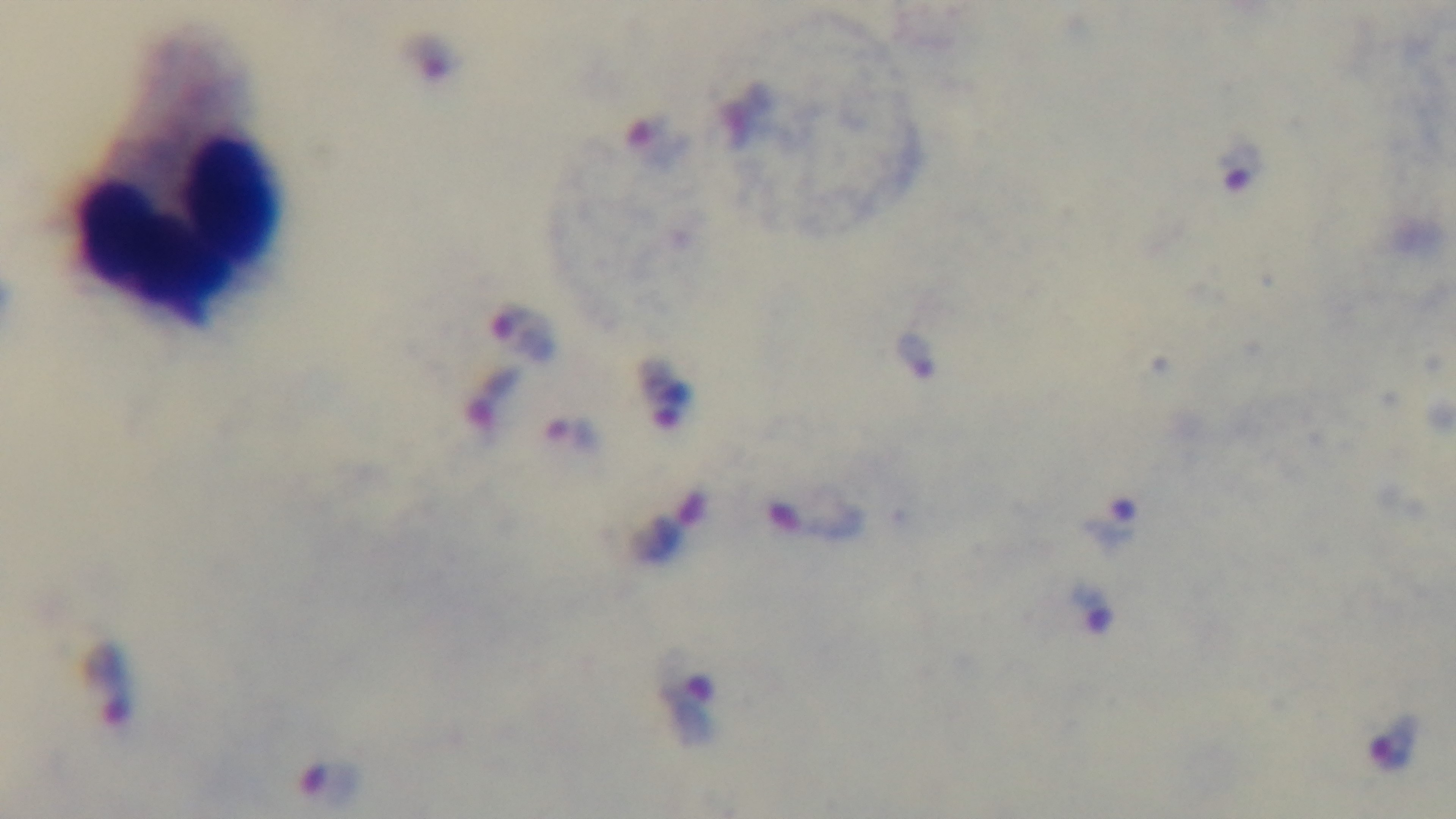 Mounted 4K digital camera. Giemsa-stained. Preparation: thick blood film. Photomicrograph. Oil-immersion objective, 100x. Malaria status: infected. Single field of view.